Locate every uninfected red blood cell.
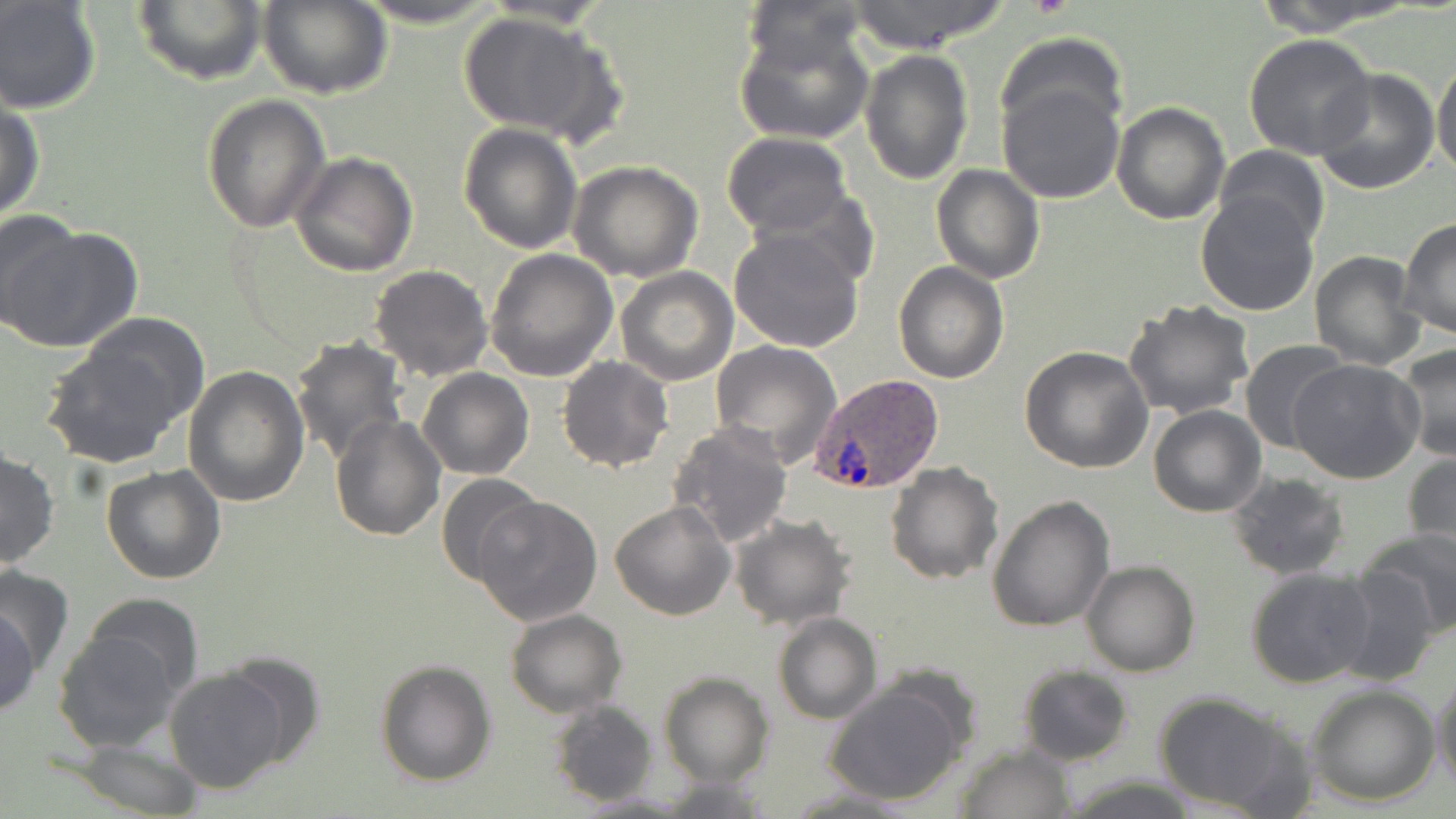
Approximate bounding boxes as named x1/y1/x2/y2 corners in pixels.
Uninfected red blood cells: (x1=258, y1=0, x2=392, y2=100), (x1=350, y1=0, x2=507, y2=28), (x1=738, y1=0, x2=873, y2=74), (x1=842, y1=0, x2=1010, y2=54), (x1=1252, y1=0, x2=1408, y2=34), (x1=0, y1=1, x2=101, y2=115), (x1=132, y1=1, x2=268, y2=87), (x1=457, y1=9, x2=620, y2=143), (x1=736, y1=20, x2=874, y2=147), (x1=1243, y1=33, x2=1376, y2=160), (x1=997, y1=36, x2=1126, y2=143), (x1=860, y1=49, x2=972, y2=184), (x1=1432, y1=56, x2=1455, y2=186), (x1=1310, y1=67, x2=1441, y2=194), (x1=998, y1=79, x2=1125, y2=204), (x1=202, y1=95, x2=330, y2=233), (x1=1111, y1=100, x2=1231, y2=224), (x1=0, y1=101, x2=45, y2=226), (x1=457, y1=121, x2=582, y2=253), (x1=720, y1=132, x2=852, y2=237), (x1=1214, y1=145, x2=1329, y2=251), (x1=291, y1=152, x2=419, y2=276), (x1=567, y1=160, x2=704, y2=282), (x1=931, y1=165, x2=1044, y2=283), (x1=754, y1=185, x2=879, y2=290), (x1=1196, y1=191, x2=1322, y2=316), (x1=3, y1=208, x2=87, y2=329), (x1=1398, y1=217, x2=1455, y2=341), (x1=0, y1=222, x2=143, y2=354), (x1=728, y1=227, x2=866, y2=354), (x1=486, y1=247, x2=618, y2=382), (x1=1309, y1=250, x2=1427, y2=369), (x1=893, y1=263, x2=1008, y2=384), (x1=369, y1=265, x2=493, y2=381), (x1=616, y1=267, x2=739, y2=386), (x1=1123, y1=300, x2=1256, y2=421), (x1=43, y1=327, x2=199, y2=467), (x1=291, y1=337, x2=409, y2=466), (x1=709, y1=339, x2=841, y2=469), (x1=1238, y1=339, x2=1350, y2=454), (x1=1398, y1=344, x2=1456, y2=462), (x1=1019, y1=346, x2=1153, y2=474), (x1=556, y1=357, x2=674, y2=473), (x1=1289, y1=358, x2=1424, y2=484), (x1=184, y1=366, x2=310, y2=507), (x1=419, y1=368, x2=533, y2=480), (x1=1148, y1=405, x2=1267, y2=516), (x1=329, y1=415, x2=446, y2=541), (x1=671, y1=423, x2=793, y2=548), (x1=0, y1=450, x2=58, y2=569), (x1=1404, y1=451, x2=1455, y2=565), (x1=885, y1=461, x2=1004, y2=585), (x1=101, y1=464, x2=228, y2=584), (x1=1227, y1=472, x2=1349, y2=580), (x1=436, y1=473, x2=546, y2=588), (x1=986, y1=494, x2=1115, y2=633), (x1=472, y1=495, x2=604, y2=627), (x1=610, y1=501, x2=736, y2=620), (x1=730, y1=513, x2=856, y2=628), (x1=1360, y1=527, x2=1455, y2=636), (x1=1082, y1=560, x2=1199, y2=676), (x1=0, y1=561, x2=74, y2=677), (x1=1244, y1=567, x2=1379, y2=689), (x1=1333, y1=567, x2=1440, y2=685), (x1=83, y1=593, x2=203, y2=700), (x1=0, y1=597, x2=42, y2=721), (x1=504, y1=609, x2=627, y2=718), (x1=772, y1=613, x2=882, y2=725), (x1=56, y1=617, x2=191, y2=747), (x1=220, y1=654, x2=327, y2=768), (x1=375, y1=658, x2=497, y2=787), (x1=164, y1=665, x2=290, y2=793), (x1=1015, y1=665, x2=1134, y2=766), (x1=1432, y1=672, x2=1455, y2=793), (x1=660, y1=674, x2=773, y2=786), (x1=823, y1=680, x2=969, y2=805), (x1=1306, y1=684, x2=1441, y2=805), (x1=1152, y1=690, x2=1312, y2=816), (x1=549, y1=700, x2=657, y2=805), (x1=70, y1=736, x2=204, y2=818), (x1=954, y1=745, x2=1074, y2=818), (x1=1057, y1=774, x2=1207, y2=817), (x1=655, y1=776, x2=776, y2=816), (x1=776, y1=786, x2=926, y2=817), (x1=569, y1=791, x2=695, y2=817).

slide-level diagnosis = Plasmodium ovale
image size = 1456×819 pixels
preparation = thin blood smear
Plasmodium ovale-infected red blood cell locations = approximate bounding boxes as named x1/y1/x2/y2 corners in pixels: (x1=810, y1=374, x2=942, y2=495)
field of view = single
magnification = 1000x
modality = light microscopy
stain = May-Grünwald-Giemsa